Assess this cell for malaria.
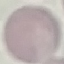
Uninfected.

Summary:
  - Image type: automatically extracted cell patch, resized to 64 × 64 pixels
  - Capture: smartphone through the microscope eyepiece
  - Stain: Giemsa
  - Preparation: thin blood film